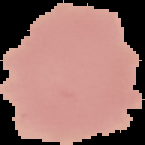
image_size: 145×145 pixels
image_type: segmented cell region with the area outside set to black
result: no Plasmodium parasites seen
preparation: thin blood smear